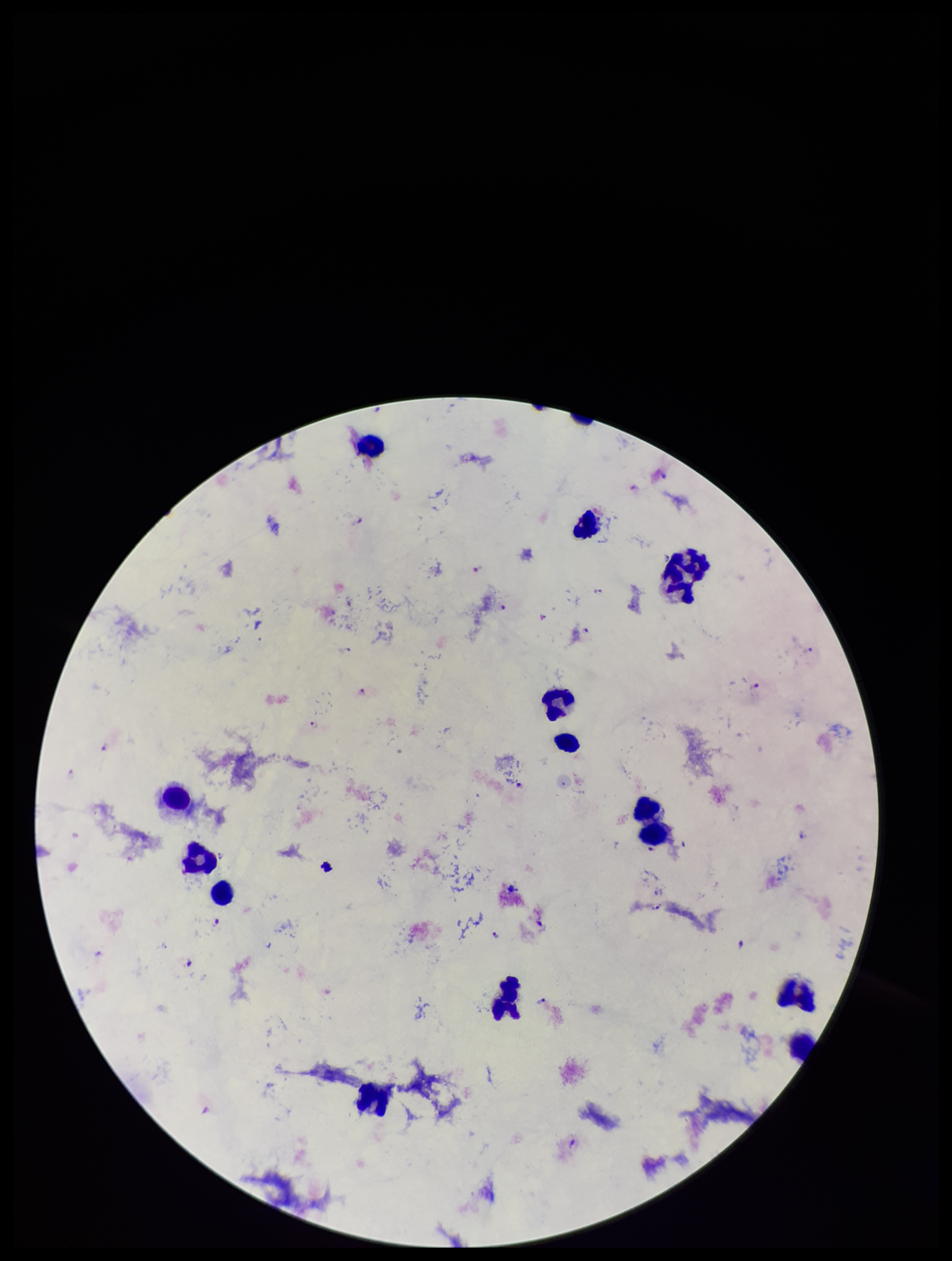

Summary:
  - Species reported for this patient: Plasmodium falciparum
  - Field of view: one from this slide
  - Preparation: thick
  - Image size: 952×1261 pixels
  - Capture: smartphone photograph through the microscope eyepiece
  - Plasmodium parasites: identified
  - Leukocyte count: 14
  - Patient malaria status: positive
  - Parasite count: 25
  - Stain: Giemsa